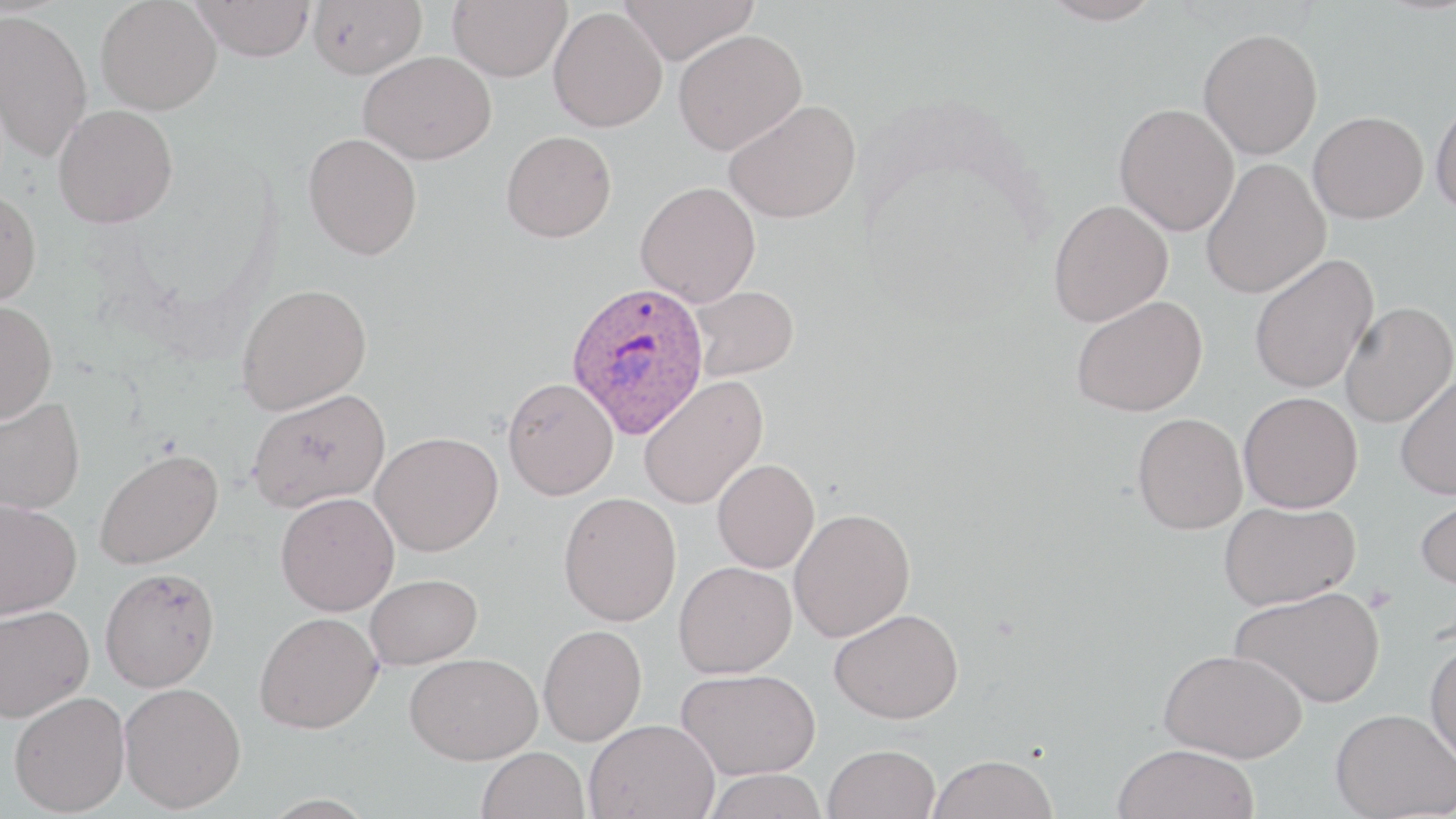 Approximate bounding boxes as (x1,y1)-(x2,y2) corner pairs in pixels. Plasmodium ovale-infected red blood cell locations: (565,280)-(711,439). Uninfected red blood cell locations: (96,0)-(222,115), (191,0)-(315,61), (307,0)-(427,79), (447,0)-(572,81), (619,0)-(759,64), (1038,0)-(1165,26), (0,8)-(93,163), (549,8)-(667,132), (1198,27)-(1323,159), (673,29)-(807,154), (359,51)-(496,165), (1430,97)-(1456,216), (724,99)-(861,224), (1114,102)-(1239,236), (53,103)-(178,229), (1308,111)-(1428,223), (501,130)-(617,242), (303,132)-(422,260), (1200,158)-(1331,299), (635,181)-(760,306), (0,186)-(42,306), (1048,199)-(1173,327), (1248,253)-(1379,395), (236,282)-(372,414), (690,284)-(799,380), (1071,294)-(1208,417), (0,299)-(57,423), (1339,301)-(1455,428), (1395,372)-(1456,500), (638,375)-(768,510), (503,377)-(618,500), (247,388)-(390,512), (1238,391)-(1363,513), (0,397)-(85,515), (1132,412)-(1247,534), (371,431)-(503,556), (94,448)-(223,569), (712,458)-(820,573), (1415,488)-(1456,591), (275,492)-(399,616), (558,492)-(682,626), (0,500)-(82,618), (1218,500)-(1360,610), (788,508)-(915,642), (674,561)-(797,678), (100,567)-(220,692), (365,573)-(482,669), (1230,585)-(1385,708), (0,604)-(93,722), (829,607)-(965,723), (254,611)-(383,733), (538,624)-(647,746), (1424,639)-(1456,766), (1159,648)-(1307,762), (405,652)-(542,764), (676,668)-(821,779), (119,682)-(246,813), (8,691)-(130,815), (1330,708)-(1455,819), (584,717)-(719,819), (824,744)-(940,819), (1112,744)-(1260,819), (477,747)-(589,819), (929,754)-(1058,819), (704,768)-(827,819). Slide-level diagnosis: Plasmodium ovale. One field of a larger specimen. Optical microscopy. Thin blood smear. Image is 1456×819 pixels. May-Grünwald-Giemsa stain. 1000x magnification.